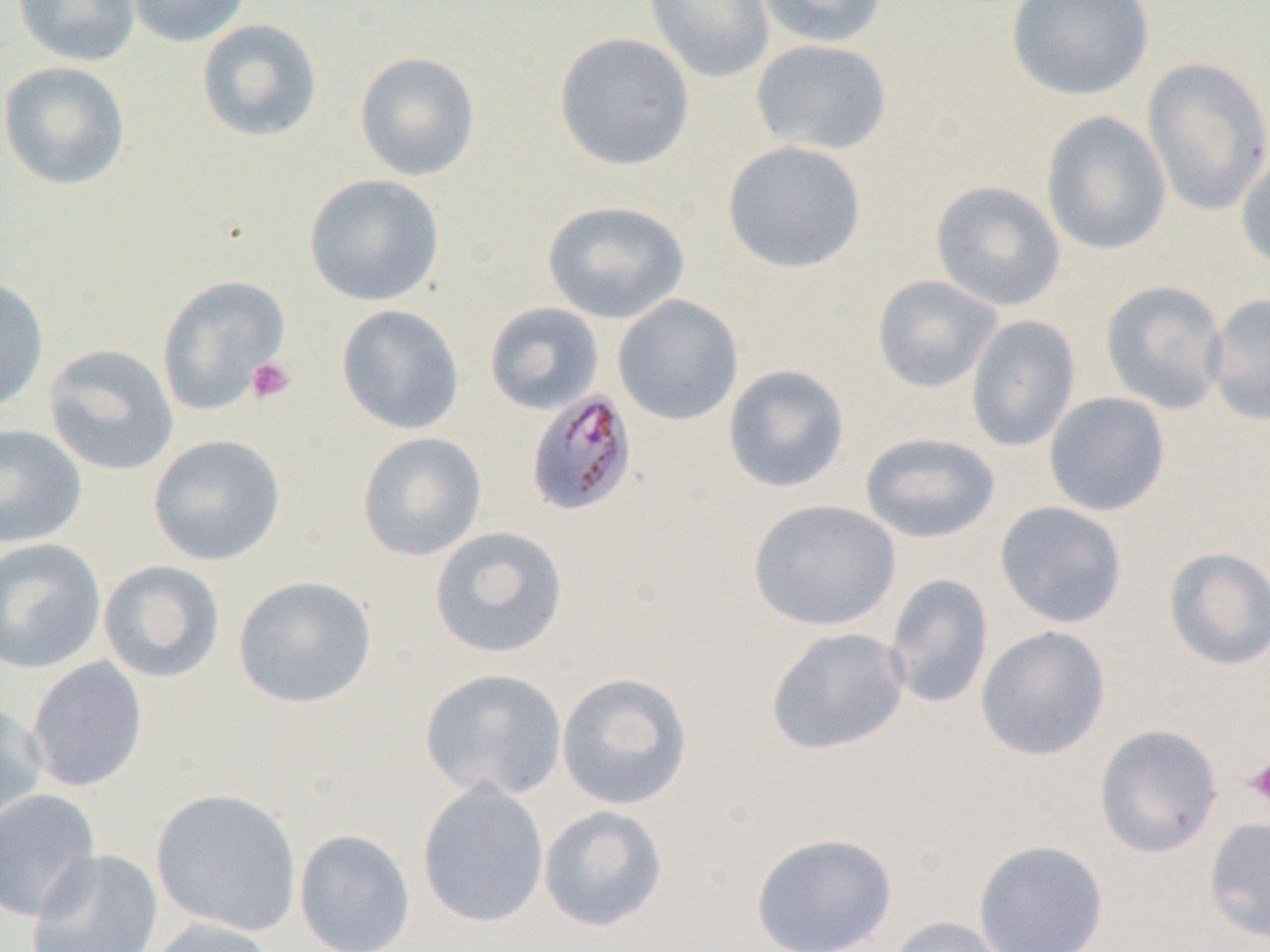
slide-level diagnosis = Plasmodium malariae
image size = 1270×952 pixels
modality = light microscopy
preparation = thin blood film
uninfected red blood cell locations = approximate bounding boxes as (x1, y1, x2, y2) in pixels: (13, 0, 141, 67), (125, 0, 251, 48), (643, 0, 775, 84), (756, 0, 888, 48), (1006, 0, 1154, 101), (196, 18, 324, 143), (554, 31, 696, 171), (750, 39, 893, 156), (354, 51, 481, 182), (1141, 56, 1270, 215), (0, 61, 132, 191), (1041, 110, 1172, 255), (723, 140, 867, 273), (1235, 147, 1270, 273), (303, 173, 445, 307), (930, 180, 1066, 312), (542, 200, 690, 324), (0, 274, 50, 414), (872, 274, 1003, 394), (156, 275, 291, 416), (1100, 279, 1228, 415), (1205, 292, 1270, 428), (612, 294, 745, 426), (484, 302, 604, 414), (336, 304, 465, 435), (966, 314, 1081, 453), (43, 344, 180, 476), (723, 364, 850, 493), (1043, 391, 1171, 517), (0, 423, 88, 548), (356, 431, 487, 562), (859, 432, 1001, 543), (148, 434, 286, 566), (747, 499, 901, 631), (994, 501, 1128, 629), (428, 525, 569, 659), (0, 537, 107, 675), (1162, 547, 1270, 671), (98, 560, 226, 684), (883, 572, 994, 710), (233, 575, 377, 709), (975, 625, 1111, 761), (765, 626, 910, 756), (26, 656, 148, 793), (420, 668, 569, 801), (556, 672, 694, 810), (0, 699, 49, 832), (1094, 723, 1222, 858), (417, 781, 550, 928), (0, 788, 102, 924), (151, 788, 303, 937), (538, 805, 669, 932), (1203, 815, 1270, 944), (294, 829, 416, 952), (750, 832, 898, 952), (973, 839, 1109, 951), (26, 848, 163, 952), (885, 916, 1014, 952), (143, 918, 281, 952)
Plasmodium malariae-infected red blood cell locations = approximate bounding boxes as (x1, y1, x2, y2) in pixels: (526, 388, 638, 516)
platelet locations = approximate bounding boxes as (x1, y1, x2, y2) in pixels: (245, 357, 296, 404), (1245, 756, 1270, 808)
magnification = 1000x
field of view = one of a larger specimen